Assess this cell for malaria.
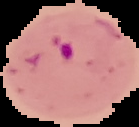

Parasitized.

Image is 139×127 pixels. From a thin blood film. Segmented cell region on a black background.